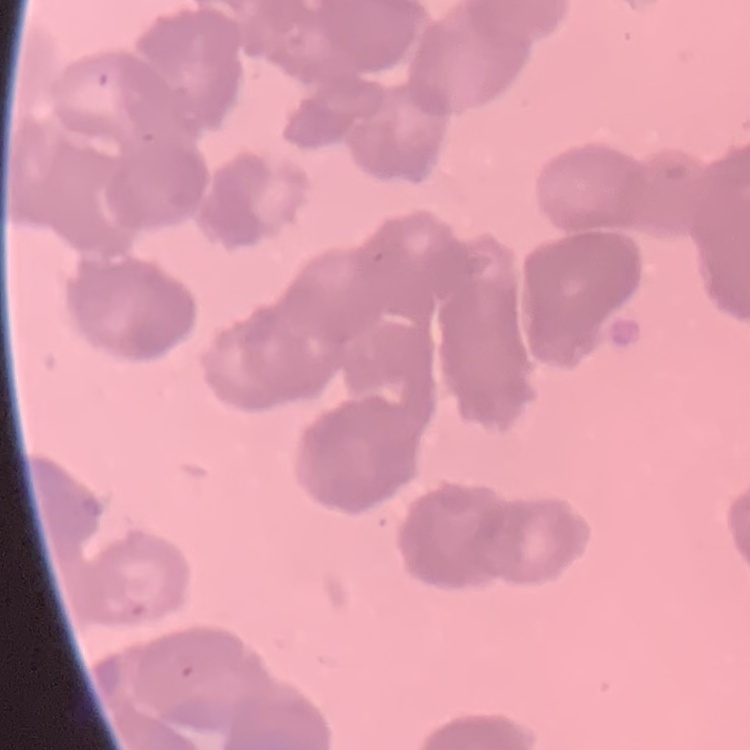

The erythrocytes show rouleaux formation. One tile cut from a larger photomicrograph. Field's or Giemsa stain. Thin blood smear.